Name the blood parasite species.
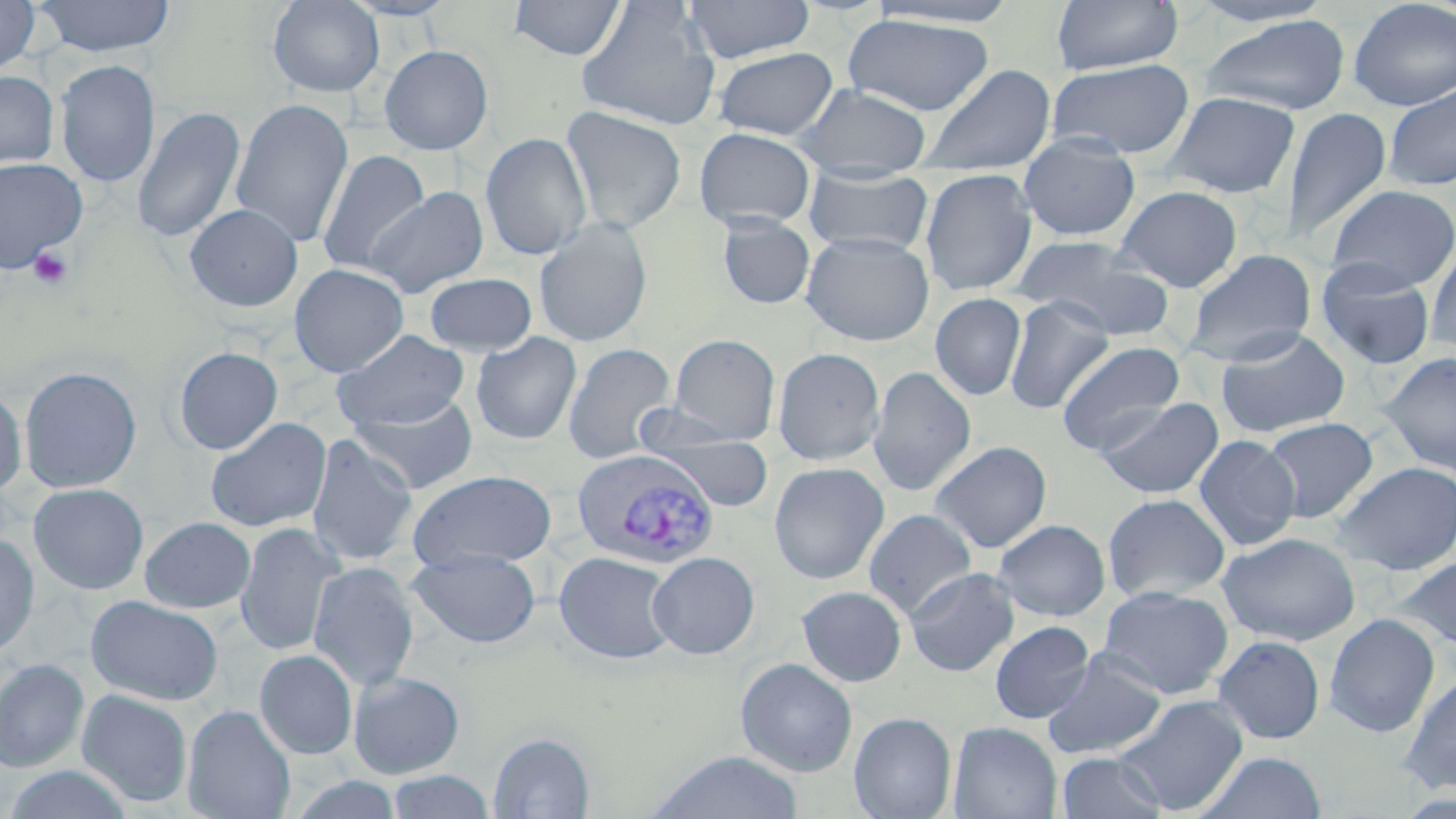
Plasmodium vivax.

field of view = one of a larger specimen
preparation = thin blood smear
modality = optical microscopy
Plasmodium vivax-infected red blood cell locations = approximate bounding boxes as named x1/y1/x2/y2 corners in pixels: (x1=570, y1=450, x2=720, y2=570)
platelet locations = approximate bounding boxes as named x1/y1/x2/y2 corners in pixels: (x1=27, y1=244, x2=75, y2=289)
magnification = 1000x
uninfected red blood cell locations = approximate bounding boxes as named x1/y1/x2/y2 corners in pixels: (x1=0, y1=0, x2=40, y2=76), (x1=33, y1=0, x2=176, y2=56), (x1=267, y1=0, x2=385, y2=98), (x1=340, y1=0, x2=460, y2=21), (x1=508, y1=0, x2=628, y2=61), (x1=682, y1=0, x2=815, y2=64), (x1=1051, y1=0, x2=1183, y2=76), (x1=1186, y1=0, x2=1338, y2=27), (x1=1347, y1=0, x2=1456, y2=111), (x1=576, y1=1, x2=721, y2=131), (x1=866, y1=1, x2=1023, y2=28), (x1=841, y1=14, x2=997, y2=116), (x1=1198, y1=15, x2=1352, y2=116), (x1=379, y1=45, x2=493, y2=155), (x1=711, y1=47, x2=840, y2=141), (x1=55, y1=59, x2=160, y2=189), (x1=1046, y1=59, x2=1195, y2=160), (x1=917, y1=64, x2=1057, y2=177), (x1=0, y1=70, x2=59, y2=171), (x1=794, y1=84, x2=932, y2=174), (x1=1384, y1=84, x2=1456, y2=191), (x1=1163, y1=92, x2=1300, y2=198), (x1=230, y1=98, x2=354, y2=249), (x1=132, y1=105, x2=246, y2=244), (x1=1281, y1=106, x2=1392, y2=245), (x1=560, y1=107, x2=687, y2=233), (x1=694, y1=128, x2=816, y2=230), (x1=480, y1=132, x2=592, y2=261), (x1=1017, y1=133, x2=1141, y2=241), (x1=316, y1=149, x2=431, y2=278), (x1=0, y1=156, x2=88, y2=273), (x1=802, y1=166, x2=934, y2=257), (x1=920, y1=167, x2=1038, y2=296), (x1=1325, y1=184, x2=1456, y2=293), (x1=1114, y1=185, x2=1243, y2=292), (x1=366, y1=186, x2=489, y2=299), (x1=184, y1=203, x2=303, y2=312), (x1=716, y1=215, x2=816, y2=309), (x1=533, y1=217, x2=653, y2=348), (x1=800, y1=232, x2=934, y2=346), (x1=1013, y1=235, x2=1175, y2=339), (x1=1425, y1=237, x2=1456, y2=356), (x1=1181, y1=249, x2=1317, y2=366), (x1=1316, y1=260, x2=1435, y2=371), (x1=289, y1=263, x2=409, y2=377), (x1=424, y1=272, x2=538, y2=355), (x1=930, y1=293, x2=1027, y2=401), (x1=1004, y1=296, x2=1115, y2=415), (x1=1215, y1=327, x2=1351, y2=438), (x1=332, y1=329, x2=469, y2=430), (x1=471, y1=332, x2=582, y2=445), (x1=668, y1=333, x2=781, y2=443), (x1=1056, y1=340, x2=1186, y2=455), (x1=563, y1=343, x2=677, y2=464), (x1=174, y1=346, x2=283, y2=454), (x1=772, y1=347, x2=885, y2=465), (x1=1379, y1=352, x2=1456, y2=477), (x1=18, y1=366, x2=142, y2=493), (x1=868, y1=366, x2=976, y2=496), (x1=0, y1=386, x2=28, y2=499), (x1=347, y1=394, x2=480, y2=495), (x1=1096, y1=397, x2=1223, y2=499), (x1=631, y1=409, x2=763, y2=478), (x1=205, y1=417, x2=331, y2=533), (x1=1261, y1=417, x2=1378, y2=523), (x1=640, y1=429, x2=776, y2=511), (x1=305, y1=433, x2=418, y2=568), (x1=1194, y1=435, x2=1301, y2=551), (x1=929, y1=441, x2=1052, y2=553), (x1=1331, y1=461, x2=1456, y2=576), (x1=769, y1=462, x2=890, y2=584), (x1=408, y1=469, x2=558, y2=570), (x1=28, y1=483, x2=149, y2=594), (x1=1102, y1=493, x2=1230, y2=604), (x1=863, y1=508, x2=977, y2=620), (x1=139, y1=516, x2=256, y2=613), (x1=994, y1=518, x2=1110, y2=621), (x1=235, y1=523, x2=343, y2=656), (x1=1217, y1=532, x2=1360, y2=646), (x1=0, y1=533, x2=40, y2=660), (x1=408, y1=549, x2=541, y2=649), (x1=554, y1=551, x2=679, y2=665), (x1=648, y1=552, x2=760, y2=659), (x1=1392, y1=556, x2=1456, y2=657), (x1=308, y1=561, x2=419, y2=692), (x1=904, y1=567, x2=1020, y2=677), (x1=796, y1=585, x2=907, y2=687), (x1=1097, y1=585, x2=1234, y2=699), (x1=86, y1=595, x2=224, y2=706), (x1=1323, y1=613, x2=1441, y2=737), (x1=990, y1=621, x2=1095, y2=724), (x1=1213, y1=635, x2=1325, y2=744), (x1=254, y1=649, x2=358, y2=759), (x1=1042, y1=650, x2=1168, y2=760), (x1=735, y1=658, x2=857, y2=777), (x1=0, y1=659, x2=89, y2=772), (x1=348, y1=671, x2=465, y2=779), (x1=1400, y1=672, x2=1456, y2=795), (x1=76, y1=688, x2=193, y2=807), (x1=1115, y1=694, x2=1249, y2=815), (x1=182, y1=704, x2=296, y2=819), (x1=849, y1=712, x2=957, y2=819), (x1=949, y1=721, x2=1062, y2=818), (x1=487, y1=732, x2=595, y2=818), (x1=647, y1=751, x2=803, y2=819), (x1=1057, y1=751, x2=1168, y2=818), (x1=1197, y1=751, x2=1326, y2=819), (x1=2, y1=766, x2=137, y2=819), (x1=385, y1=770, x2=496, y2=818)
stain = May-Grünwald-Giemsa
image size = 1456×819 pixels